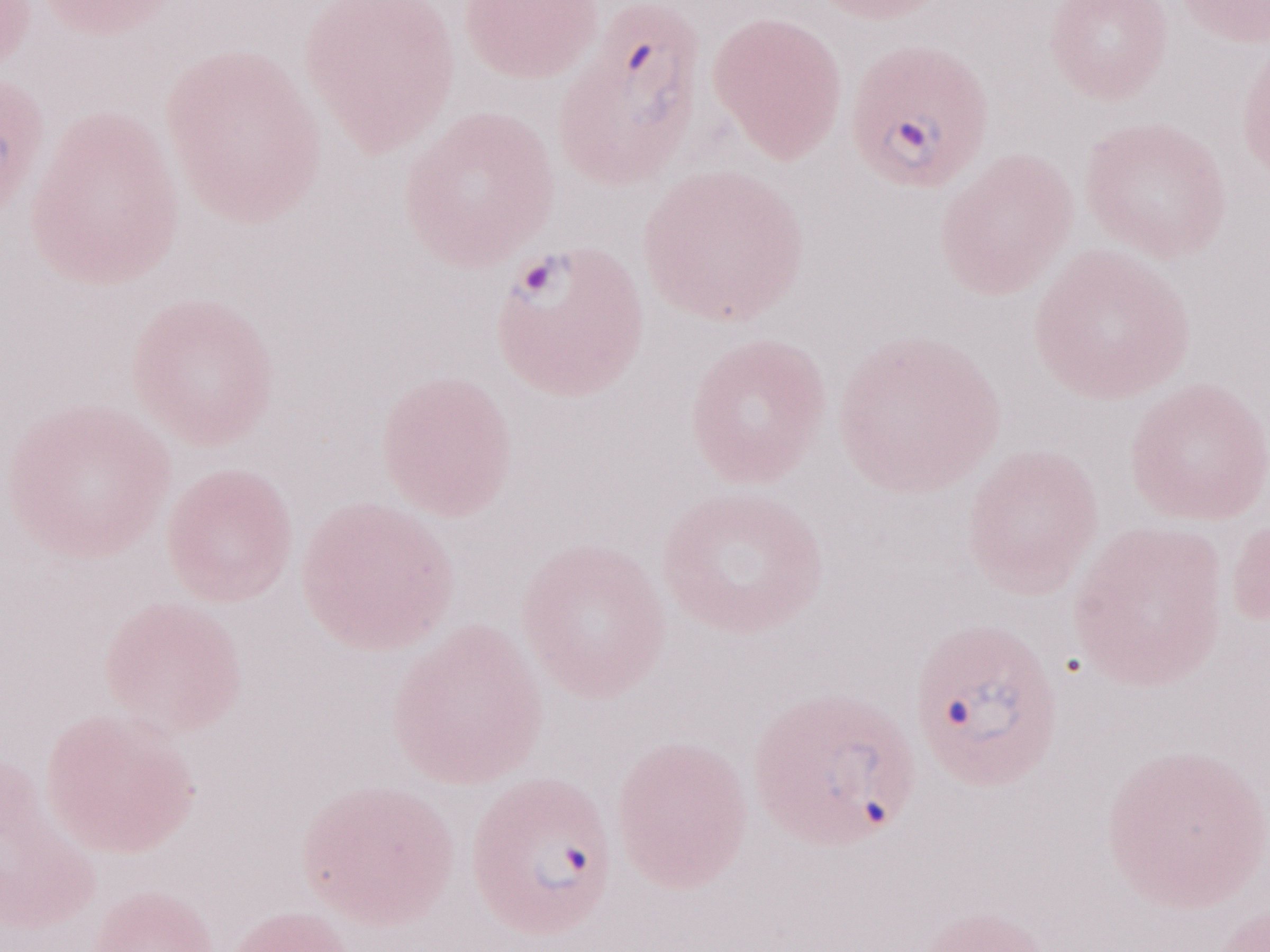 Thin blood film. One field of this slide. Magnification: 1,000x. Image is 1270×952 pixels. May-Grünwald-Giemsa stain. Olympus BX43 microscope and DP73 digital camera. Malaria diagnosis (patient-level): positive.